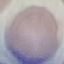

Summary:
  - Malaria status: uninfected
  - Stain: Giemsa
  - Preparation: thin blood film
  - Capture: smartphone camera at the microscope eyepiece
  - Image type: cell patch, automatically extracted from a larger field of view and resized to 64 × 64 pixels